Identify the parasite.
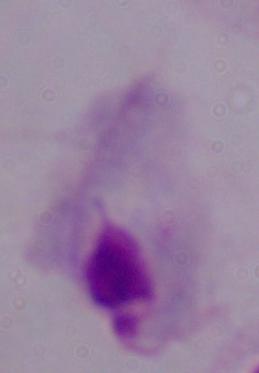
A trichomonad.

magnification = 1000x
modality = micrograph